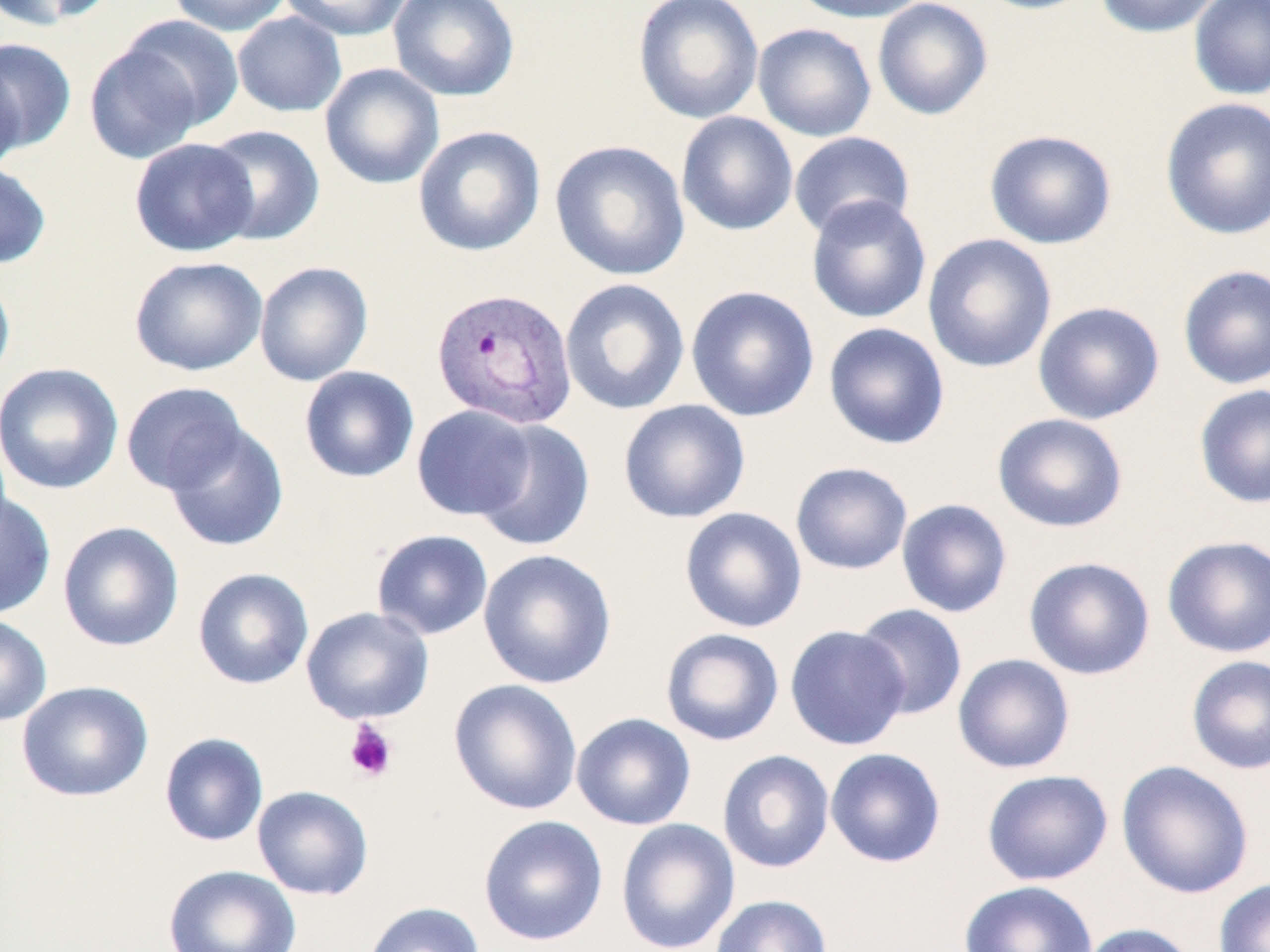
Approximate bounding boxes as (x1,y1)-(x2,y2) corner pairs in pixels. Plasmodium vivax-infected red blood cell locations: (431,287)-(578,430). Platelet locations: (343,719)-(399,783). Uninfected red blood cell locations: (1,0)-(110,32), (167,0)-(292,36), (279,0)-(412,41), (388,0)-(520,102), (633,0)-(764,124), (787,0)-(932,24), (872,0)-(993,120), (972,0)-(1101,15), (1094,0)-(1222,38), (1188,0)-(1270,101), (232,11)-(347,117), (118,14)-(244,131), (752,22)-(876,142), (0,38)-(77,154), (84,42)-(205,164), (0,59)-(26,174), (319,63)-(445,190), (1159,97)-(1270,241), (676,111)-(798,236), (204,124)-(326,245), (412,125)-(546,257), (984,129)-(1117,250), (788,131)-(916,240), (129,137)-(259,257), (550,139)-(690,282), (0,160)-(52,269), (805,195)-(932,324), (922,233)-(1057,373), (129,255)-(268,376), (254,261)-(373,386), (1177,264)-(1270,390), (0,269)-(16,390), (559,278)-(690,415), (686,285)-(820,422), (1033,301)-(1165,424), (823,322)-(950,450), (0,362)-(124,495), (299,366)-(420,483), (121,381)-(247,495), (1193,383)-(1270,510), (618,398)-(751,524), (411,404)-(537,521), (992,413)-(1128,533), (471,420)-(595,552), (164,423)-(289,553), (790,461)-(913,575), (0,490)-(56,619), (896,498)-(1013,618), (680,506)-(807,633), (57,520)-(185,652), (371,529)-(494,641), (1161,535)-(1270,658), (477,548)-(618,689), (1023,556)-(1155,680), (192,567)-(314,690), (852,603)-(968,721), (300,606)-(435,725), (0,613)-(52,727), (785,624)-(910,750), (660,628)-(785,746), (952,653)-(1076,774), (1186,655)-(1270,775), (448,678)-(583,815), (16,680)-(154,802), (571,712)-(696,830), (159,732)-(269,846), (825,747)-(946,868), (717,749)-(835,873), (1116,760)-(1254,899), (981,769)-(1113,885), (252,785)-(374,901), (478,815)-(609,946), (615,818)-(740,952), (163,864)-(301,952), (1214,878)-(1270,952), (958,880)-(1098,952), (710,894)-(833,952), (362,901)-(486,952), (1077,922)-(1200,952). Slide-level diagnosis: Plasmodium vivax. Image is 1270×952 pixels. Light microscopy. Captured at 1000x magnification. One field of a larger specimen. May-Grünwald-Giemsa stain. Thin blood film.